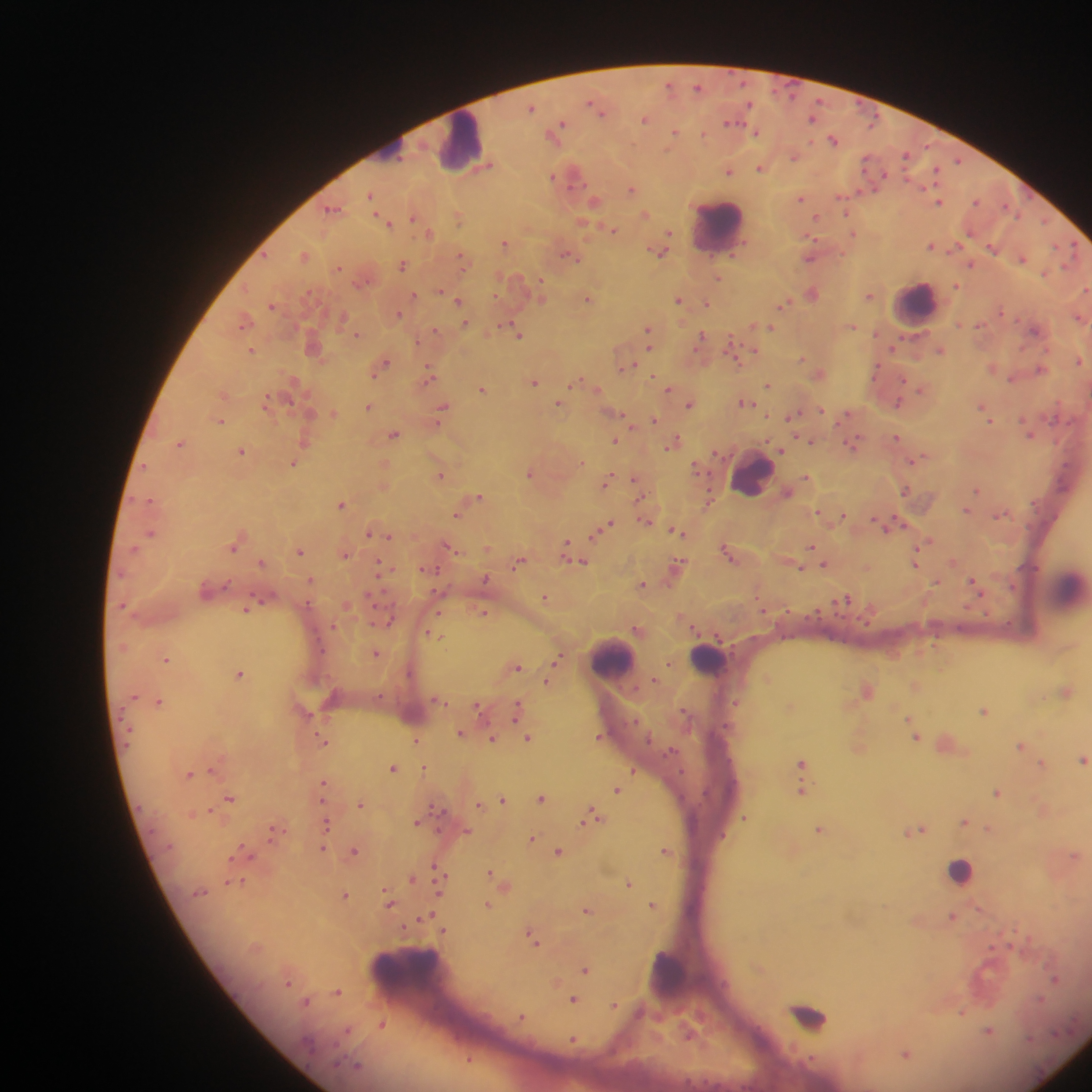
Approximate centers as x y in pixels.
Summary:
  - Leukocyte locations: 462 142; 719 224; 917 303; 753 473; 614 658; 708 660; 960 871; 668 973; 813 1015
  - Malaria parasite locations: 669 85; 697 86; 749 104; 532 107; 597 108; 601 112; 813 119; 645 120; 730 123; 559 128; 674 132; 756 132; 556 135; 703 135; 833 140; 793 156; 906 156; 867 160; 958 161; 489 165; 760 168; 935 170; 730 171; 574 175; 552 176; 631 189; 370 196; 800 198; 976 201; 594 202; 843 202; 939 202; 333 208; 845 211; 646 214; 412 217; 458 218; 816 218; 387 221; 1044 221; 613 229; 429 233; 853 233; 669 234; 505 243; 931 246; 993 247; 659 252; 734 252; 304 256; 568 256; 810 258; 1023 259; 464 261; 970 264; 403 265; 339 268; 1045 273; 718 278; 540 284; 956 286; 1085 290; 812 293; 415 295; 869 295; 541 298; 588 299; 678 300; 458 302; 708 303; 784 304; 271 306; 1002 312; 399 313; 1078 317; 342 319; 243 322; 464 324; 978 325; 852 326; 512 328; 770 328; 648 330; 1034 330; 437 331; 356 334; 518 334; 702 336; 649 340; 731 342; 894 346; 252 351; 940 351; 755 352; 802 358; 1079 360; 383 364; 628 365; 1040 368; 429 373; 1011 379; 578 380; 904 380; 534 382; 768 384; 597 388; 482 389; 921 389; 669 390; 745 402; 899 402; 266 403; 559 404; 690 404; 982 406; 369 407; 442 407; 820 410; 984 412; 333 413; 794 414; 619 415; 846 415; 654 419; 989 420; 220 421; 394 435; 1029 435; 896 438; 615 441; 811 441; 673 442; 179 443; 852 444; 781 450; 241 451; 915 460; 581 463; 294 464; 695 467; 530 473; 440 475; 806 477; 608 478; 636 484; 905 490; 977 490; 787 492; 479 497; 151 500; 709 500; 341 504; 966 510; 818 512; 457 514; 843 514; 999 515; 645 520; 875 522; 891 524; 605 526; 678 531; 597 532; 151 533; 368 533; 388 536; 929 540; 566 545; 448 546; 233 547; 811 547; 299 551; 727 552; 345 554; 519 562; 581 562; 260 563; 825 564; 915 564; 677 565; 382 566; 800 568; 430 570; 485 579; 311 580; 936 582; 643 584; 974 585; 546 598; 847 598; 762 608; 246 609; 484 613; 389 622; 435 634; 376 653; 166 659; 559 659; 668 664; 518 667; 239 674; 655 679; 547 681; 1066 691; 159 702; 736 703; 479 706; 517 710; 983 710; 685 712; 909 719; 912 729; 460 732; 599 737; 527 738; 916 738; 415 740; 492 740; 324 742; 1020 746; 1083 759; 801 763; 1042 763; 394 768; 424 768; 211 769; 634 771; 189 774; 324 784; 617 791; 802 791; 996 793; 230 797; 542 798; 503 800; 480 804; 361 805; 210 811; 592 817; 743 818; 417 821; 964 822; 327 824; 920 829; 989 829; 819 830; 274 831; 467 832; 531 839; 323 848; 354 851; 665 851; 246 852; 558 852; 1074 856; 437 867; 489 872; 412 879; 440 880; 242 882; 629 882; 232 883; 345 895; 389 904; 488 905; 652 905; 586 911; 425 916; 952 916; 405 928; 443 930; 533 937; 585 970; 1055 980; 338 992; 1040 999; 572 1000; 307 1002; 614 1006; 962 1012; 520 1017; 382 1025; 348 1031; 989 1031; 573 1041; 906 1055; 469 1060
  - Image size: 1092×1092 pixels
  - Country: Ghana
  - Capture: mobile-phone photograph through a microscope
  - Preparation: thick blood smear
  - Field of view: single